Give the preparation type.
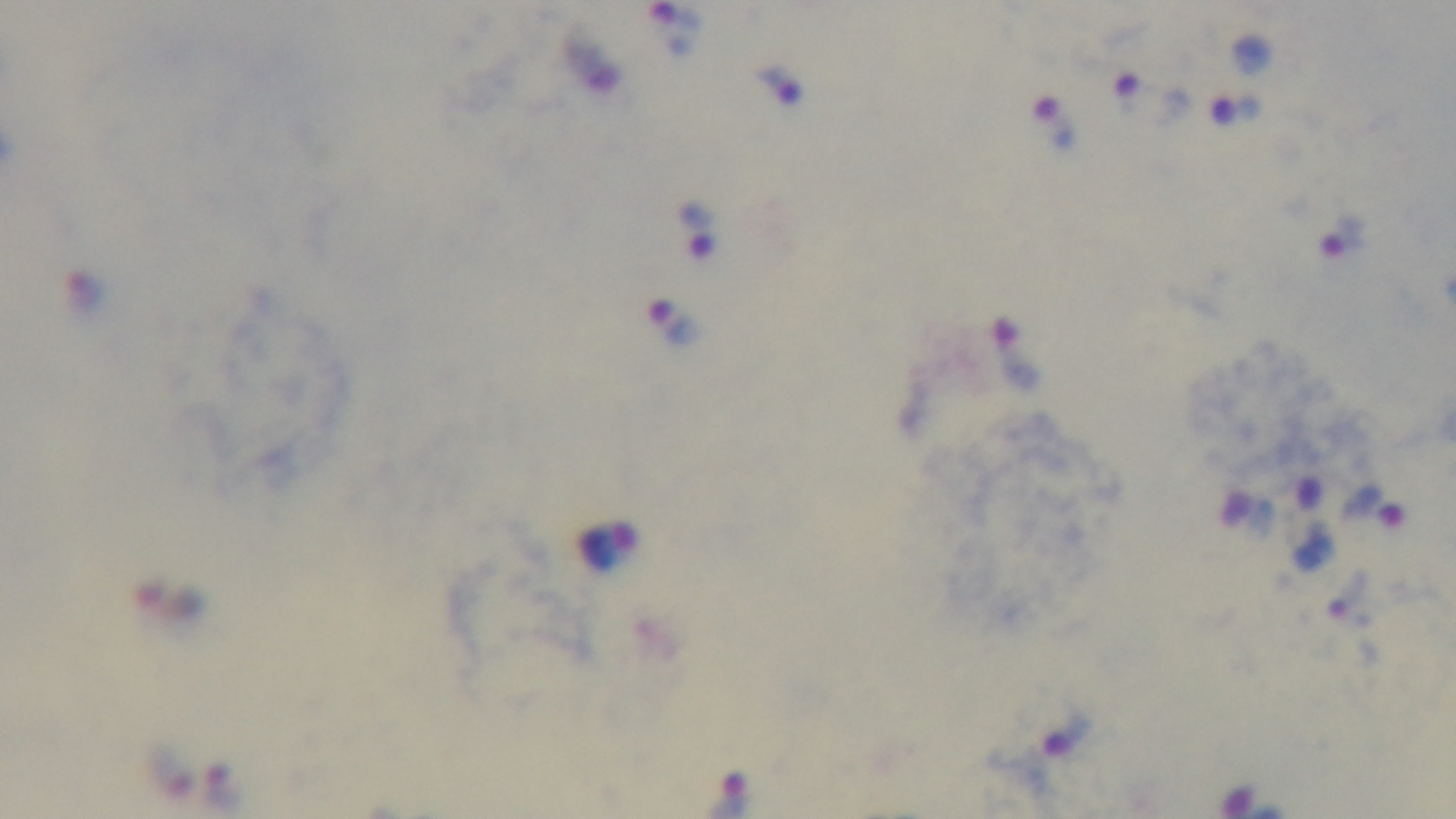
A thick smear.

Giemsa stain. 100x oil-immersion objective. Malaria status: infected. Photomicrograph. Mounted 4K digital camera. Single field of view.